Classify this cell by malaria status.
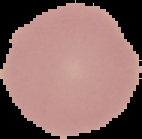
It is uninfected.

{
  "image_type": "segmented cell region on a black background",
  "image_size": "142×139 pixels",
  "preparation": "thin blood smear"
}